Locate platelets.
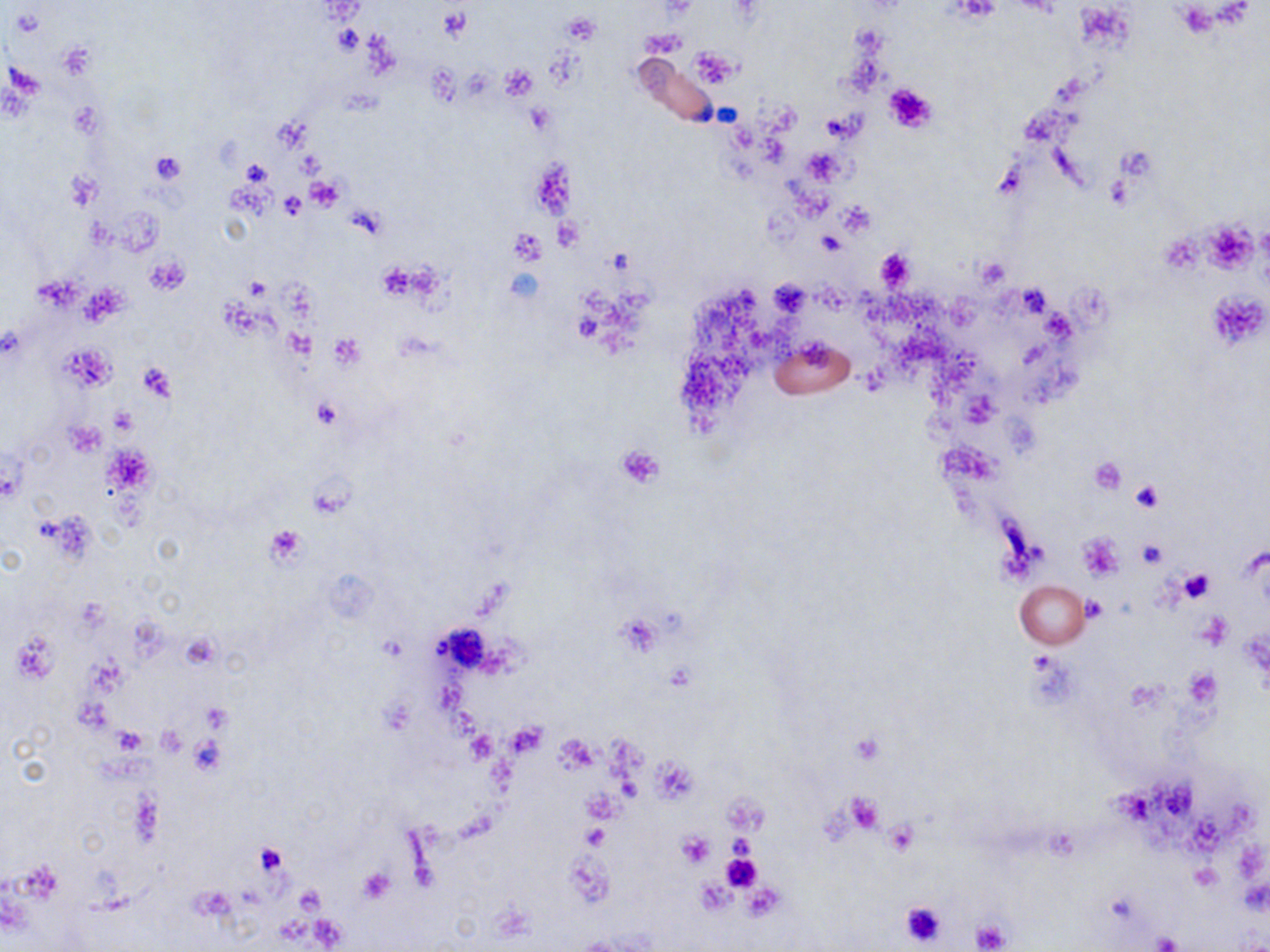
Approximate bounding boxes as (x1,y1)-(x2,y2) corner pairs in pixels.
Platelets: (949,0)-(1001,23), (439,7)-(473,42), (562,13)-(600,45), (333,25)-(364,53), (641,30)-(686,57), (690,48)-(740,88), (500,66)-(537,102), (883,82)-(939,134), (70,99)-(105,138), (527,104)-(556,133), (822,113)-(857,141), (1115,145)-(1159,183), (804,148)-(846,184), (149,151)-(185,183), (529,157)-(576,224), (240,160)-(271,187), (68,171)-(103,210), (305,179)-(344,211), (279,192)-(304,218), (836,202)-(875,237), (554,216)-(582,250), (1203,222)-(1257,273), (509,229)-(546,265), (816,230)-(845,255), (874,247)-(914,293), (147,255)-(189,294), (973,256)-(1011,291), (378,260)-(420,301), (245,277)-(271,300), (769,280)-(811,316), (1208,290)-(1269,352), (329,334)-(364,371), (137,361)-(175,400), (312,398)-(342,430), (109,407)-(136,434), (66,421)-(105,456), (107,442)-(154,496), (616,446)-(665,488), (1089,458)-(1126,495), (1131,479)-(1163,511), (265,524)-(308,565), (1077,533)-(1124,583), (1137,538)-(1166,568), (1180,567)-(1215,604), (1081,595)-(1108,622), (1198,611)-(1231,650), (10,632)-(59,684), (178,634)-(221,670), (1183,669)-(1220,710), (506,721)-(546,758), (156,725)-(186,757), (112,727)-(148,755), (466,730)-(498,764), (555,734)-(599,772), (849,734)-(885,765), (190,736)-(229,775), (654,758)-(697,802), (843,793)-(886,834), (884,821)-(919,856), (582,823)-(609,851), (677,832)-(715,868), (255,845)-(287,876), (720,850)-(762,892), (1191,864)-(1222,891), (356,866)-(394,904), (740,883)-(784,919), (899,900)-(947,946), (971,920)-(1007,952), (1154,931)-(1183,952).

slide-level diagnosis = negative for blood parasites
preparation = thin blood film
magnification = 1000x
uninfected red blood cell locations = approximate bounding boxes as (x1,y1)-(x2,y2) corner pairs in pixels: (769,335)-(856,399), (1015,580)-(1089,649)
modality = light microscopy
stain = May-Grünwald-Giemsa
field of view = one of a larger specimen
image size = 1270×952 pixels